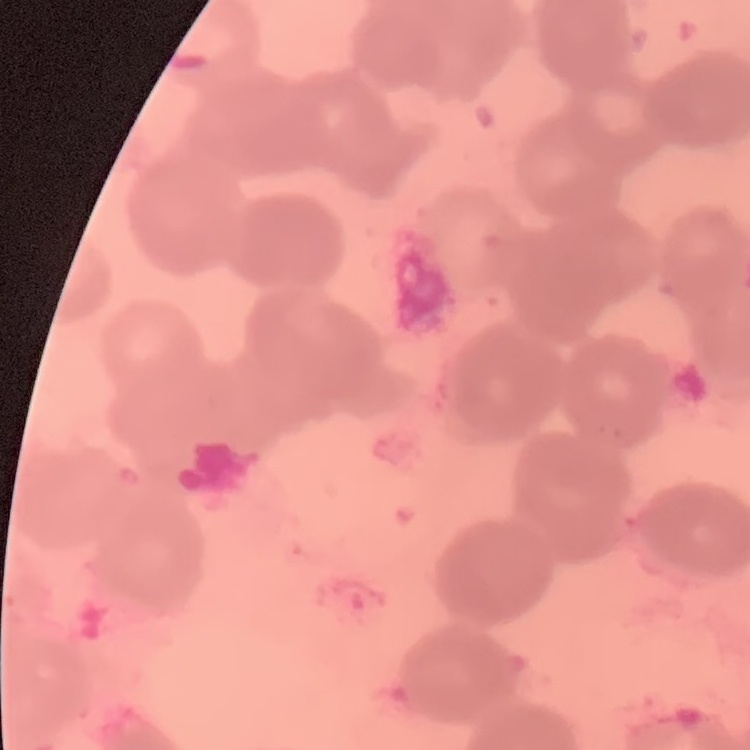
Summary:
  - Erythrocyte morphology: rouleaux formation
  - Preparation: thin blood film
  - Stain: Field's or Giemsa
  - Image type: one tile cut from a larger photomicrograph